Outline each Plasmodium malariae-infected red blood cell.
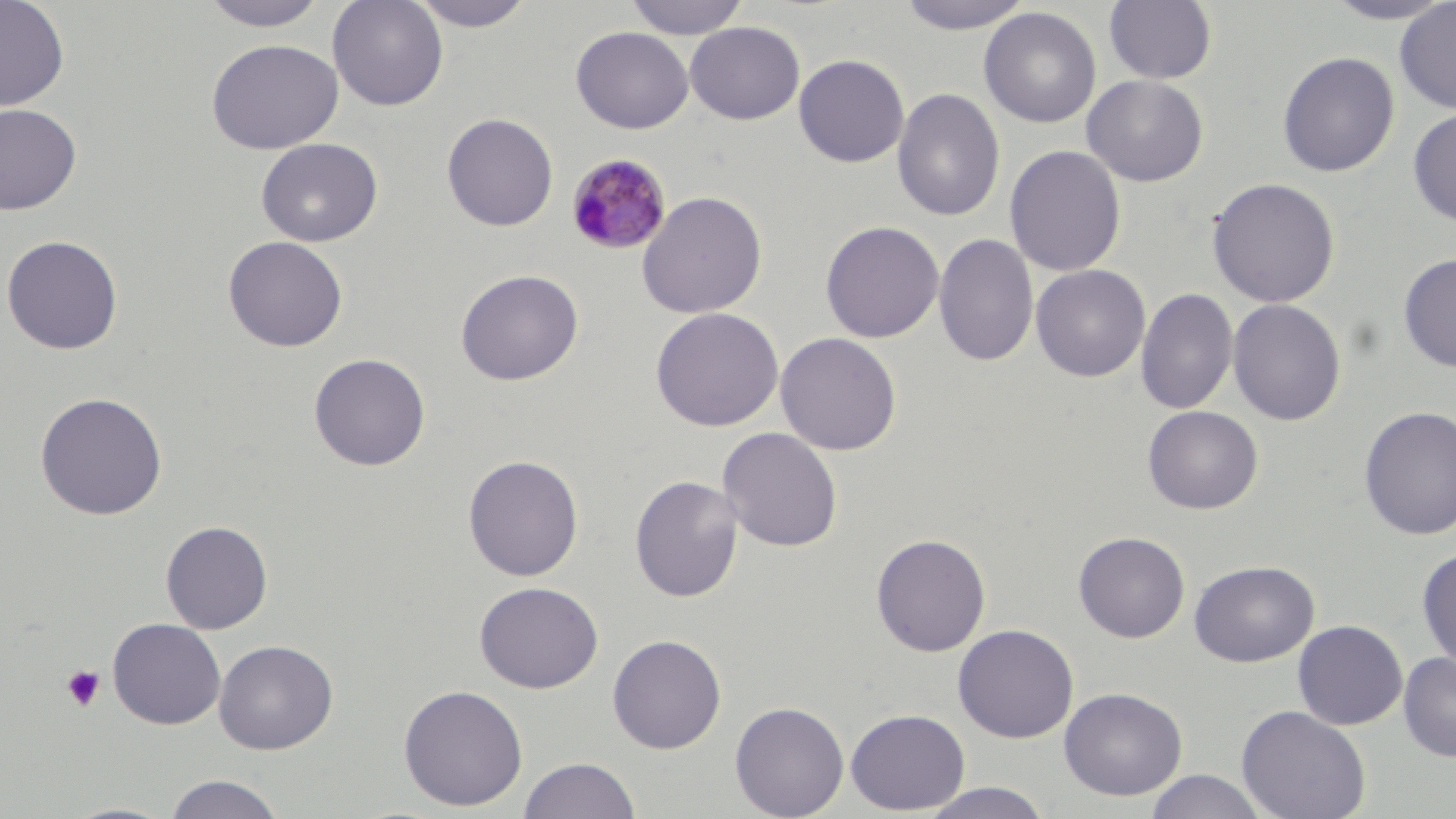
Approximate bounding boxes as (x1,y1)-(x2,y2) corner pairs in pixels.
Plasmodium malariae-infected red blood cells: (566,153)-(673,255).

Platelet locations: (61,665)-(106,712). Uninfected red blood cell locations: (0,0)-(70,111), (327,0)-(449,111), (409,0)-(536,31), (623,0)-(751,39), (893,0)-(1036,34), (1103,0)-(1218,85), (1319,0)-(1456,25), (199,1)-(329,31), (1394,1)-(1456,115), (978,7)-(1102,128), (684,21)-(805,124), (571,26)-(694,133), (205,38)-(343,154), (1277,51)-(1400,177), (793,54)-(909,167), (1082,74)-(1208,187), (892,87)-(1005,222), (0,103)-(82,215), (1408,107)-(1456,227), (442,113)-(558,232), (256,137)-(383,247), (1005,145)-(1127,277), (1206,177)-(1340,307), (636,190)-(768,319), (820,221)-(944,343), (933,232)-(1039,367), (1,234)-(123,355), (223,235)-(348,352), (1398,254)-(1456,373), (1030,264)-(1151,382), (455,268)-(584,386), (1136,288)-(1238,416), (1227,298)-(1346,426), (650,307)-(784,432), (775,332)-(902,455), (308,352)-(431,471), (34,391)-(168,520), (1142,405)-(1263,514), (1358,405)-(1456,540), (717,426)-(843,552), (463,454)-(584,581), (629,475)-(744,602), (160,520)-(273,633), (1073,531)-(1190,642), (871,533)-(991,656), (1416,547)-(1456,671), (1189,560)-(1318,667), (474,580)-(604,693), (107,617)-(226,730), (1293,619)-(1408,730), (953,623)-(1079,743), (607,634)-(726,754), (213,639)-(338,754), (1397,652)-(1456,762), (398,683)-(528,811), (1059,687)-(1187,801), (729,700)-(850,819), (1236,705)-(1371,819), (845,708)-(970,815), (518,756)-(640,818), (1144,770)-(1269,819), (162,773)-(286,818), (917,782)-(1055,819), (59,801)-(180,819). Slide-level diagnosis: Plasmodium malariae. Light microscopy. Single field of view. May-Grünwald-Giemsa-stained preparation. Thin blood smear. Captured at 1000x magnification. Image is 1456×819 pixels.